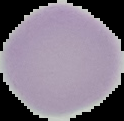

Summary:
  - Preparation: thin blood film
  - Malaria status: uninfected
  - Image size: 124×121 pixels
  - Image type: segmented cell region on a black background